Point out each Plasmodium parasite.
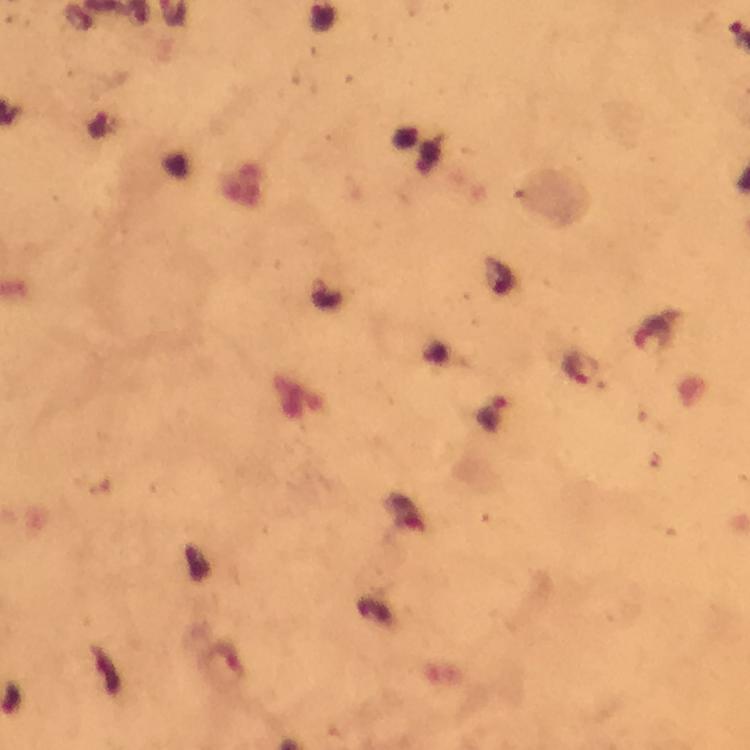

Approximate centers as (x, y) in pixels.
Plasmodium parasites: (581, 370), (492, 414).

Thick blood film. Giemsa-stained preparation. Image is 750×750 pixels. Photographed through the microscope with a smartphone camera. From a malaria diagnostic workup. 100x magnification. Cropped region of a single field of view. Immersion oil was used.